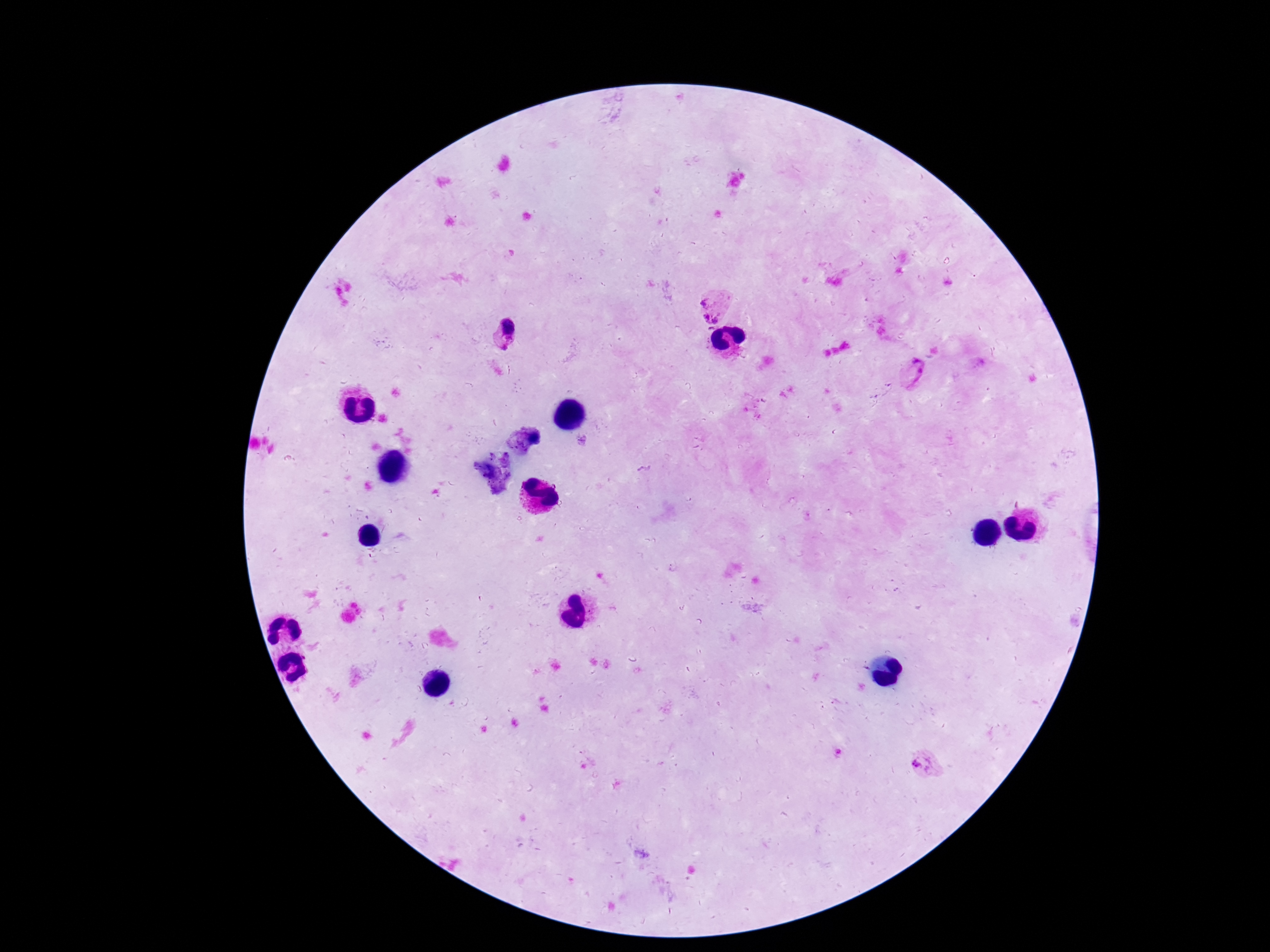

Approximate centers as {x, y} in pixels.
Summary:
  - Plasmodium parasite locations: {713, 307}, {508, 329}, {915, 371}, {924, 764}
  - Image size: 1270×952 pixels
  - Capture: smartphone camera through the microscope eyepiece
  - Preparation: thick blood smear
  - Patient malaria status: positive
  - Stain: Giemsa
  - Magnification: 100x
  - Field of view: single